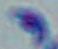

Summary:
  - Modality: micrograph
  - Identification: Toxoplasma gondii
  - Magnification: 1000x